State which cell type is depicted.
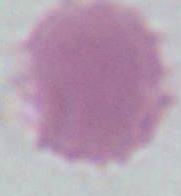

An erythrocyte.

Captured at 1000x magnification. Micrograph.